Report the malaria status of this cell.
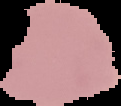

Uninfected.

{
  "image_type": "segmented cell region on a black background",
  "preparation": "thin blood film",
  "image_size": "121×106 pixels"
}